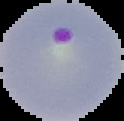
malaria_status: parasitized
preparation: thin blood film
image_size: 124×121 pixels
image_type: segmented cell region with the area outside set to black